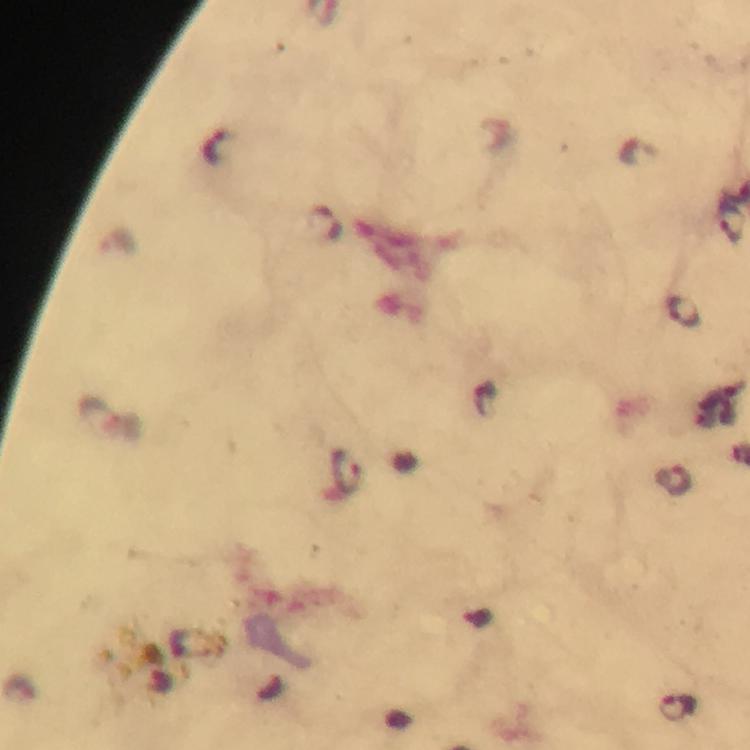

Approximate centers as [x, y] in pixels. Malaria parasite locations: [217, 148], [731, 222], [325, 224], [682, 310], [347, 468], [675, 479], [678, 709]. From a malaria diagnostic workup. Immersion oil applied. Thick blood film. Giemsa-stained preparation. At 100x magnification. A crop from one field of view. Smartphone photograph taken through a microscope. Image is 750×750 pixels.